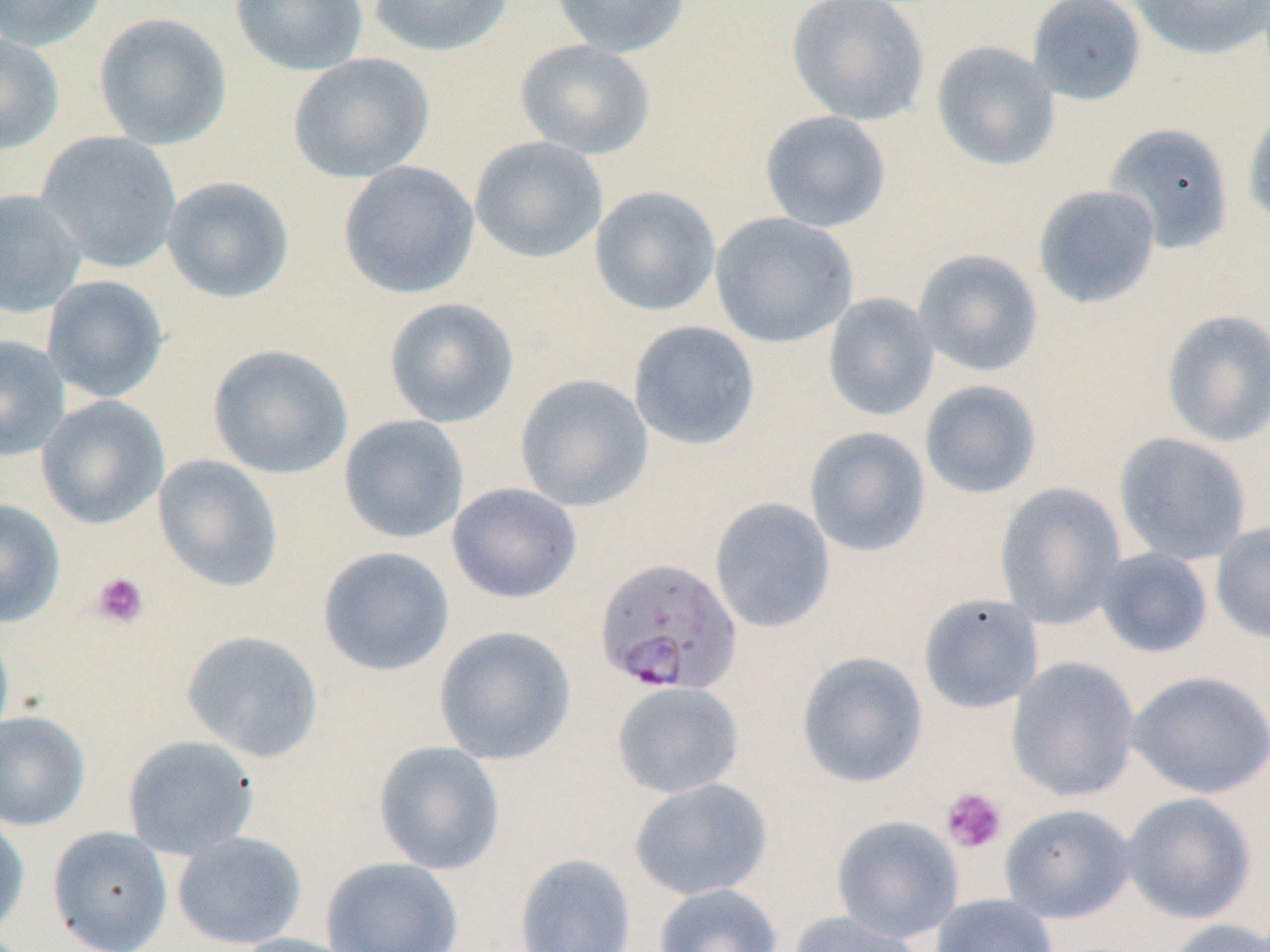
slide-level diagnosis = Plasmodium falciparum
platelet locations = approximate bounding boxes as (x1, y1, x2, y2) in pixels: (91, 572, 150, 629), (940, 787, 1007, 854)
field of view = one of a larger specimen
preparation = thin blood film
modality = optical microscopy
Plasmodium falciparum-infected red blood cell locations = approximate bounding boxes as (x1, y1, x2, y2) in pixels: (594, 556, 743, 696)
image size = 1270×952 pixels
stain = May-Grünwald-Giemsa
magnification = 1000x
uninfected red blood cell locations = approximate bounding boxes as (x1, y1, x2, y2) in pixels: (0, 0, 108, 50), (228, 0, 369, 76), (368, 0, 514, 58), (550, 0, 691, 57), (786, 0, 931, 126), (1026, 0, 1147, 105), (1128, 0, 1270, 60), (93, 12, 232, 150), (0, 33, 65, 155), (514, 39, 656, 159), (930, 40, 1060, 172), (288, 52, 434, 183), (1242, 106, 1270, 228), (759, 110, 891, 232), (1103, 122, 1234, 253), (35, 131, 182, 274), (469, 136, 608, 264), (337, 160, 480, 299), (161, 176, 295, 304), (1032, 184, 1160, 309), (589, 186, 721, 317), (0, 189, 87, 319), (709, 212, 858, 348), (912, 248, 1044, 377), (41, 274, 169, 403), (822, 292, 939, 422), (383, 297, 519, 428), (1160, 308, 1270, 448), (628, 320, 761, 450), (0, 335, 70, 462), (207, 344, 353, 479), (514, 373, 653, 512), (919, 380, 1042, 499), (35, 395, 170, 530), (338, 414, 469, 544), (804, 426, 931, 558), (1113, 431, 1252, 565), (153, 455, 283, 593), (447, 482, 582, 604), (995, 482, 1126, 629), (709, 496, 836, 634), (0, 498, 66, 627), (1210, 520, 1270, 644), (317, 546, 455, 676), (1094, 547, 1214, 659), (917, 593, 1045, 714), (0, 624, 14, 748), (433, 624, 576, 765), (181, 629, 324, 763), (796, 651, 928, 788), (1006, 657, 1140, 802), (1126, 670, 1270, 800), (611, 680, 744, 799), (0, 710, 90, 831), (122, 734, 260, 860), (374, 741, 505, 875), (629, 777, 774, 900), (1121, 792, 1257, 925), (999, 803, 1135, 924), (0, 812, 30, 940), (831, 814, 964, 943), (47, 826, 173, 952), (172, 831, 307, 949), (514, 853, 636, 952), (321, 856, 463, 952), (653, 883, 783, 952), (931, 893, 1059, 952), (785, 910, 926, 952), (1163, 918, 1270, 952), (227, 933, 363, 952)